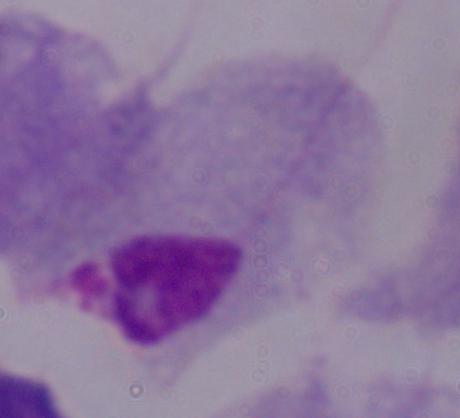
1000x magnification. A trichomonad is seen. Photomicrograph.